Identify the cell.
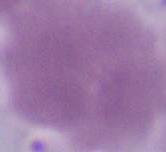

An erythrocyte.

Micrograph. 1000x magnification.